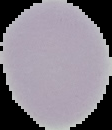
Segmented cell region on a black background. From a thin blood smear. Image is 112×130 pixels. Result: negative for malaria parasites.